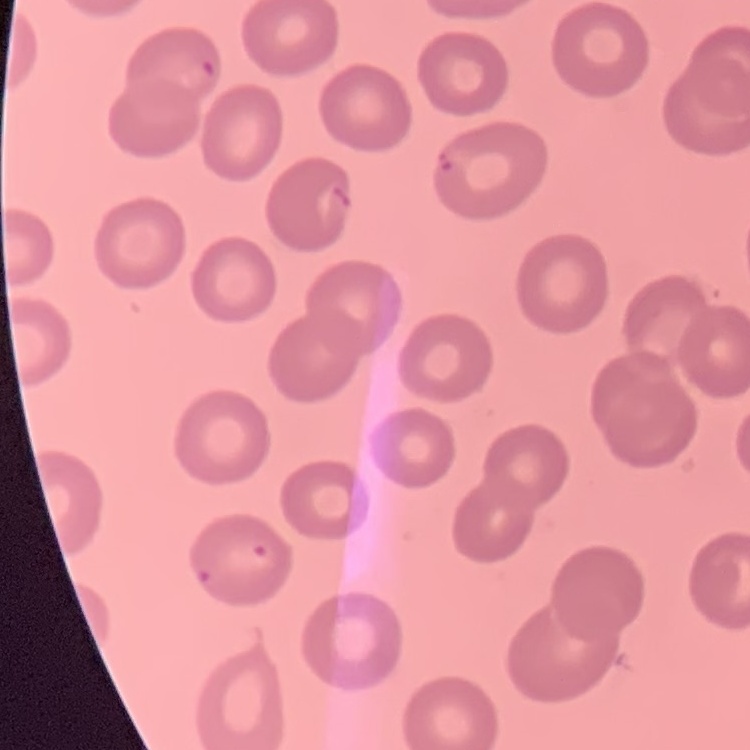

The erythrocytes show no rouleaux formation. Stained with either Field's or Giemsa. Square crop of a larger photomicrograph. Thin peripheral smear.